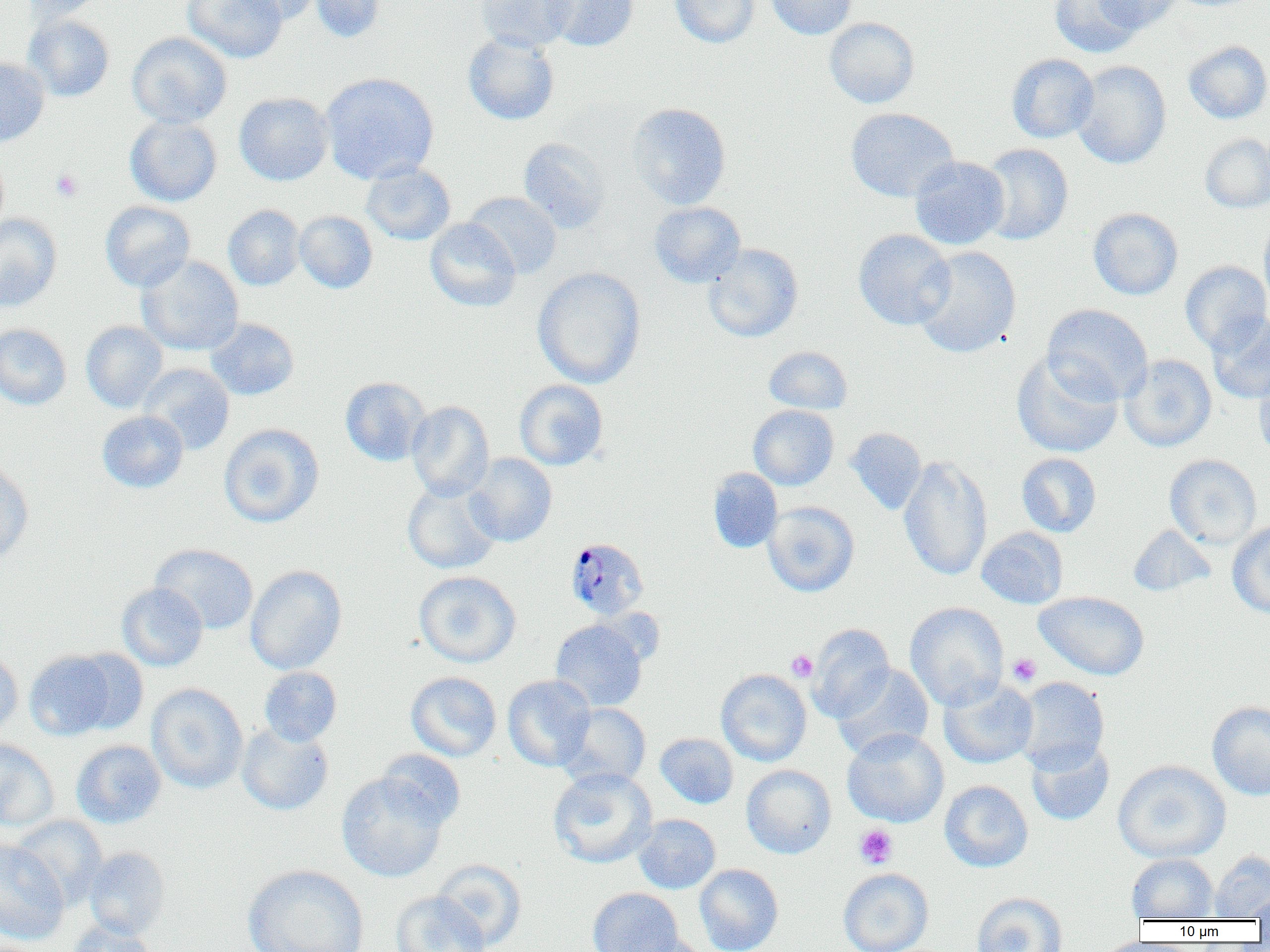
slide-level diagnosis = Plasmodium malariae
modality = optical microscopy
Plasmodium malariae-infected red blood cell locations = approximate bounding boxes as (x1,y1)-(x2,y2) corner pairs in pixels: (568,543)-(652,625)
image size = 1270×952 pixels
preparation = thin blood smear
magnification = 1000x
field of view = single
uninfected red blood cell locations = approximate bounding boxes as (x1,y1)-(x2,y2) corner pairs in pixels: (21,0)-(107,22), (183,0)-(287,63), (227,0)-(321,25), (310,0)-(385,43), (476,0)-(577,52), (544,0)-(638,51), (670,0)-(760,48), (765,0)-(857,39), (1051,0)-(1146,58), (1093,0)-(1182,32), (24,14)-(114,102), (824,17)-(920,108), (126,32)-(232,128), (463,32)-(559,125), (1183,40)-(1270,124), (1006,53)-(1099,143), (0,56)-(50,149), (1070,60)-(1171,169), (320,72)-(439,184), (234,92)-(333,186), (627,102)-(731,209), (846,107)-(959,202), (125,115)-(222,206), (1200,133)-(1270,213), (518,137)-(611,234), (978,143)-(1073,245), (0,149)-(9,238), (909,156)-(1010,250), (361,162)-(456,246), (463,192)-(562,279), (99,201)-(196,292), (649,202)-(746,288), (223,205)-(305,291), (1088,208)-(1183,300), (294,210)-(377,293), (0,213)-(62,313), (1259,215)-(1270,311), (425,218)-(521,312), (853,229)-(956,330), (703,243)-(804,343), (913,246)-(1021,358), (137,255)-(244,356), (1180,260)-(1270,354), (532,266)-(646,389), (1042,304)-(1153,403), (1208,312)-(1270,404), (205,318)-(299,400), (81,321)-(168,413), (0,324)-(71,409), (764,345)-(852,414), (1011,351)-(1123,458), (1120,354)-(1217,452), (138,363)-(235,455), (1253,364)-(1270,462), (340,377)-(431,466), (514,379)-(608,470), (406,400)-(494,500), (748,405)-(839,490), (96,411)-(189,493), (219,424)-(324,528), (845,427)-(926,514), (1017,452)-(1102,537), (466,453)-(557,547), (1164,454)-(1262,549), (898,455)-(993,581), (0,459)-(34,563), (708,468)-(783,553), (402,480)-(501,574), (763,501)-(860,597), (1227,521)-(1270,618), (1128,524)-(1216,597), (976,527)-(1068,609), (150,543)-(259,635), (244,564)-(347,674), (414,571)-(521,667), (117,582)-(208,671), (1034,591)-(1150,681), (905,602)-(1009,711), (550,619)-(647,712), (806,624)-(895,723), (68,648)-(150,734), (24,649)-(119,740), (0,650)-(23,737), (833,663)-(934,761), (259,666)-(342,746), (715,668)-(812,767), (405,671)-(502,761), (502,675)-(596,771), (938,677)-(1038,769), (1013,677)-(1110,773), (147,683)-(248,794), (1207,701)-(1270,800), (557,703)-(652,788), (236,722)-(334,816), (842,728)-(949,827), (655,733)-(738,808), (0,738)-(59,831), (71,739)-(166,828), (1026,739)-(1114,825), (378,750)-(466,829), (1113,760)-(1231,864), (741,765)-(836,859), (548,767)-(657,868), (336,772)-(449,882), (939,780)-(1033,872), (633,813)-(720,894), (10,815)-(108,909), (0,839)-(69,944), (83,847)-(170,939), (1209,851)-(1270,920), (1127,854)-(1217,921), (432,859)-(526,951), (242,864)-(369,952), (695,864)-(784,952), (838,867)-(934,952), (587,887)-(683,951), (1248,890)-(1270,923), (390,891)-(490,952), (971,892)-(1068,952), (66,919)-(157,951), (620,934)-(710,952)
platelet locations = approximate bounding boxes as (x1,y1)-(x2,y2) corner pairs in pixels: (50,168)-(83,202), (786,650)-(818,682), (1007,654)-(1041,685), (855,824)-(898,869)